Identify the blood parasite species.
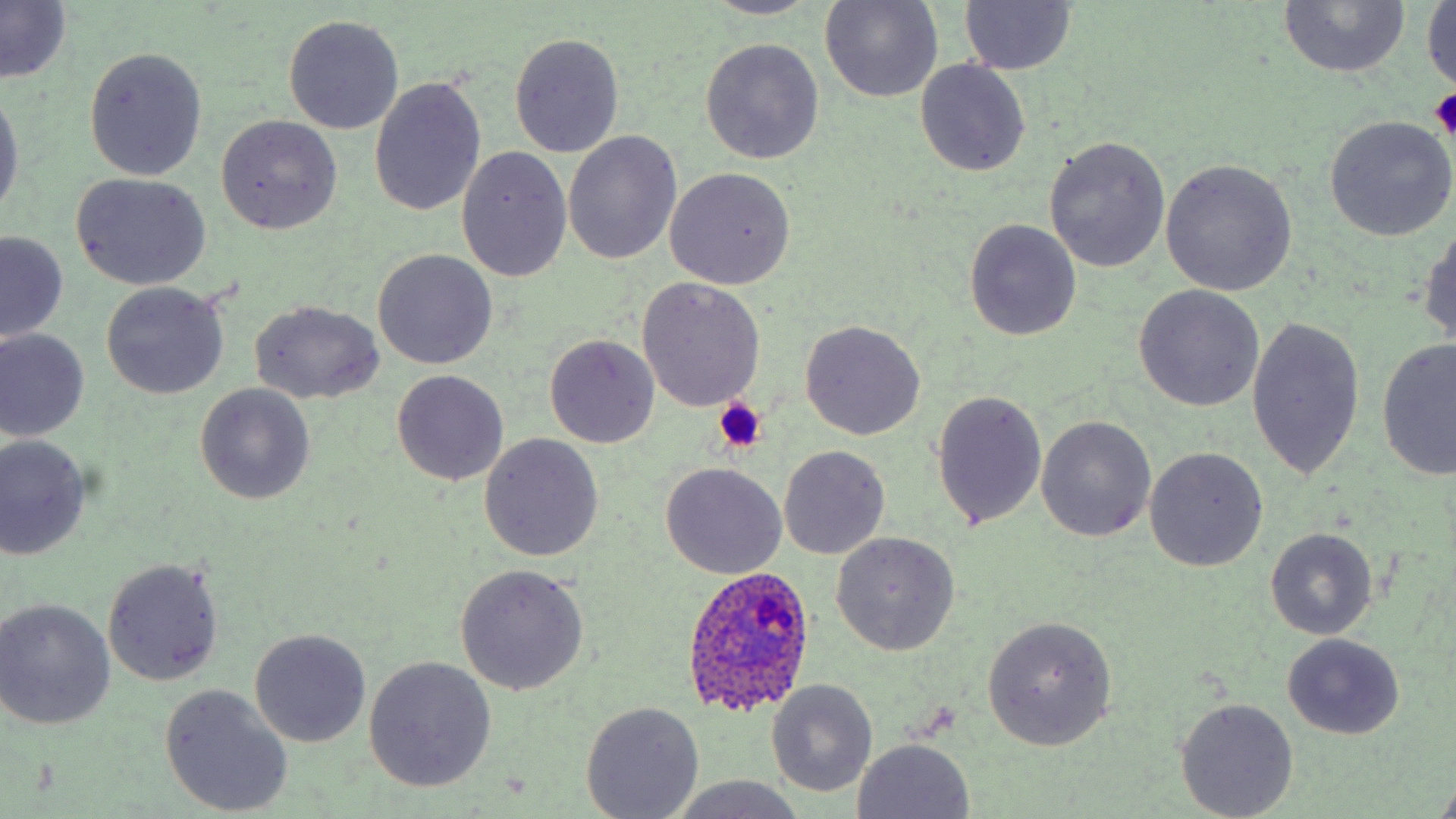

Plasmodium ovale.

Approximate bounding boxes as [x1, y1, x2, y2] in pixels. Uninfected red blood cell locations: [699, 0, 822, 19], [820, 1, 943, 104], [1277, 1, 1409, 78], [959, 2, 1077, 75], [1424, 2, 1456, 96], [0, 3, 71, 84], [283, 14, 405, 134], [510, 32, 624, 158], [700, 38, 825, 164], [83, 47, 208, 181], [915, 60, 1031, 179], [368, 77, 487, 217], [0, 89, 23, 219], [216, 116, 343, 234], [1324, 117, 1455, 242], [563, 132, 681, 265], [1042, 135, 1170, 272], [457, 146, 572, 282], [1159, 160, 1296, 297], [665, 167, 798, 289], [70, 172, 211, 291], [1419, 216, 1456, 356], [964, 219, 1081, 341], [0, 231, 68, 344], [373, 249, 497, 369], [636, 278, 766, 412], [100, 283, 229, 399], [1134, 285, 1262, 410], [250, 300, 384, 402], [1246, 315, 1366, 482], [799, 319, 926, 440], [1, 328, 90, 441], [544, 334, 659, 449], [1378, 339, 1455, 481], [390, 370, 511, 486], [195, 383, 315, 504], [931, 389, 1048, 531], [1036, 415, 1156, 543], [480, 434, 604, 561], [0, 435, 92, 560], [778, 444, 890, 560], [1145, 447, 1268, 571], [660, 462, 788, 578], [1265, 528, 1378, 638], [830, 531, 961, 655], [102, 557, 225, 685], [454, 564, 590, 695], [0, 598, 117, 729], [983, 616, 1117, 749], [249, 628, 371, 747], [1281, 634, 1405, 740], [363, 656, 497, 793], [766, 680, 878, 798], [160, 684, 294, 816], [1176, 697, 1299, 818], [581, 701, 705, 818], [850, 738, 976, 819], [666, 776, 804, 819]. Plasmodium ovale-infected red blood cell locations: [680, 566, 814, 717]. Platelet locations: [1428, 88, 1456, 139], [712, 399, 768, 452]. Optical microscopy. 1000x magnification. May-Grünwald-Giemsa-stained preparation. One field of a larger specimen. Image is 1456×819 pixels. Thin blood smear.